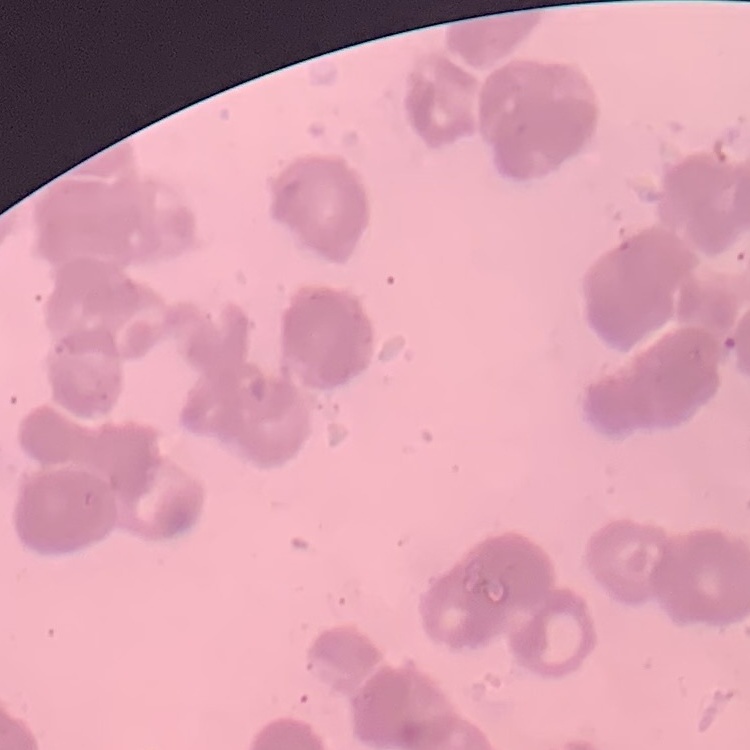

The red blood cells show rouleaux formation. Thin blood smear. One tile cut from a larger photomicrograph. Field's or Giemsa stain.